Point out each Plasmodium parasite and each leukocyte.
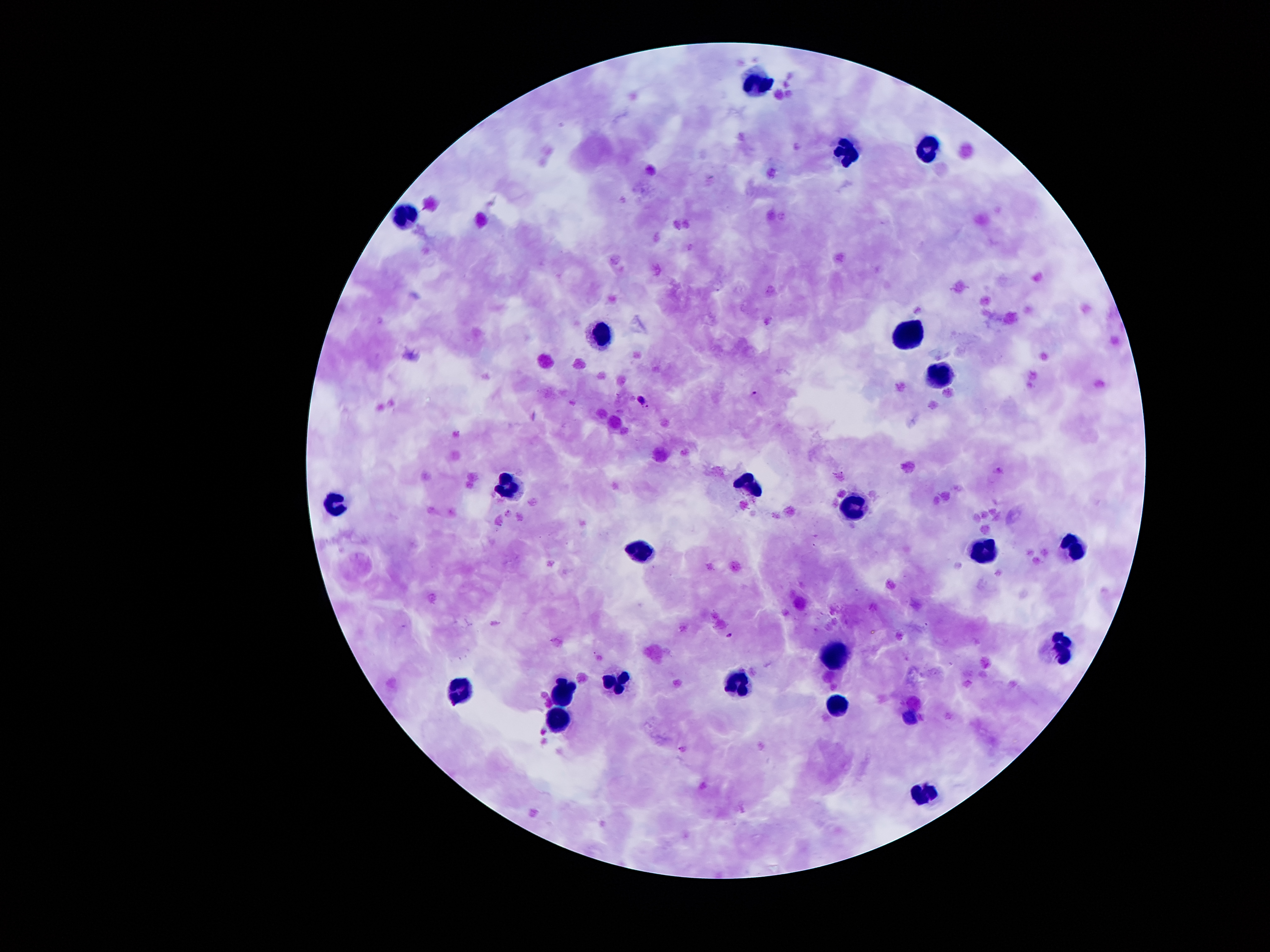

Approximate centers as (x, y) in pixels.
Plasmodium parasites: (757, 392), (642, 397), (730, 634).
Leukocytes: (757, 79), (929, 146), (844, 152), (409, 213), (909, 332), (602, 337), (941, 373), (505, 482), (748, 483), (330, 496), (853, 503), (1075, 545), (638, 549), (985, 551), (1061, 648), (836, 650), (740, 679), (617, 682), (463, 687), (564, 687), (839, 709), (907, 717), (559, 719), (924, 790).

Summary:
  - Field of view: one from this slide
  - Preparation: thick peripheral-blood smear
  - Patient malaria status: positive for Plasmodium falciparum
  - Magnification: 100x
  - Capture: smartphone through the microscope eyepiece
  - Image size: 1270×952 pixels
  - Stain: Giemsa